Locate every blood parasite and identify its species.
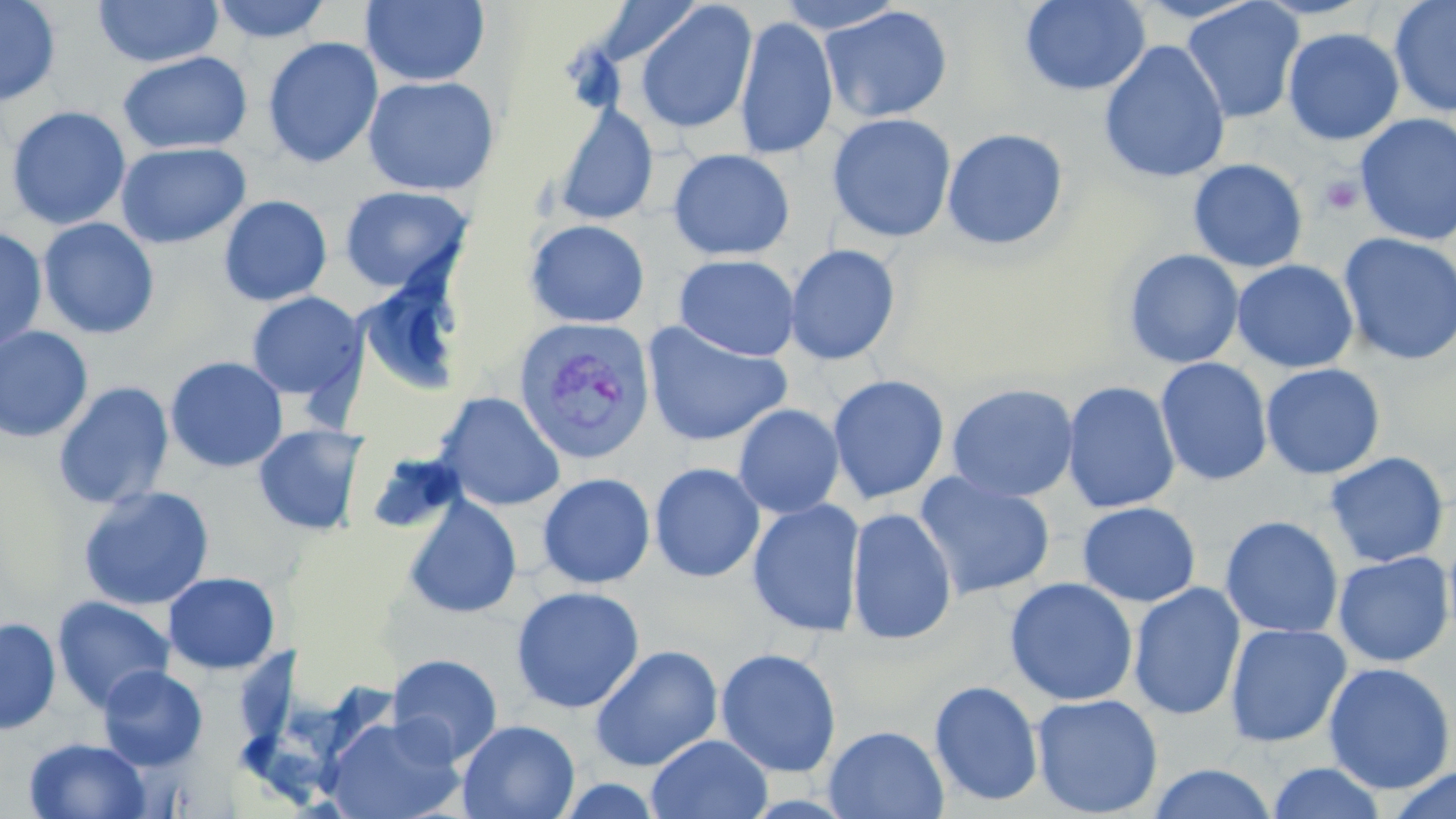

Approximate bounding boxes as named x1/y1/x2/y2 corners in pixels.
Plasmodium vivax-infected red blood cells: (x1=513, y1=317, x2=655, y2=465).
No Plasmodium falciparum, Plasmodium ovale, Plasmodium malariae, Babesia divergens, or Trypanosoma brucei observed.

slide_level_diagnosis: Plasmodium vivax
uninfected_red_blood_cell_locations: 'approximate bounding boxes as named x1/y1/x2/y2 corners in pixels: (x1=0, y1=0, x2=61, y2=107), (x1=93, y1=0, x2=223, y2=68), (x1=209, y1=0, x2=332, y2=43), (x1=774, y1=0, x2=907, y2=34), (x1=1020, y1=0, x2=1150, y2=96), (x1=1389, y1=0, x2=1456, y2=118), (x1=360, y1=1, x2=490, y2=87), (x1=587, y1=1, x2=708, y2=67), (x1=1181, y1=1, x2=1304, y2=124), (x1=633, y1=2, x2=758, y2=135), (x1=819, y1=5, x2=954, y2=124), (x1=734, y1=15, x2=838, y2=160), (x1=1282, y1=27, x2=1405, y2=146), (x1=262, y1=37, x2=383, y2=169), (x1=1098, y1=40, x2=1231, y2=185), (x1=117, y1=51, x2=253, y2=154), (x1=362, y1=75, x2=500, y2=196), (x1=552, y1=103, x2=659, y2=226), (x1=6, y1=106, x2=132, y2=230), (x1=827, y1=113, x2=957, y2=243), (x1=1355, y1=114, x2=1456, y2=246), (x1=941, y1=127, x2=1069, y2=251), (x1=116, y1=142, x2=251, y2=249), (x1=667, y1=148, x2=794, y2=261), (x1=1188, y1=158, x2=1309, y2=272), (x1=339, y1=185, x2=474, y2=294), (x1=218, y1=195, x2=333, y2=306), (x1=37, y1=217, x2=160, y2=339), (x1=525, y1=219, x2=650, y2=328), (x1=0, y1=227, x2=48, y2=353), (x1=1337, y1=232, x2=1456, y2=366), (x1=785, y1=244, x2=902, y2=366), (x1=1122, y1=248, x2=1244, y2=369), (x1=674, y1=254, x2=800, y2=361), (x1=1232, y1=259, x2=1358, y2=373), (x1=354, y1=273, x2=469, y2=398), (x1=245, y1=292, x2=367, y2=404), (x1=641, y1=320, x2=793, y2=447), (x1=0, y1=325, x2=94, y2=443), (x1=164, y1=356, x2=289, y2=473), (x1=1155, y1=357, x2=1274, y2=487), (x1=1260, y1=363, x2=1386, y2=480), (x1=827, y1=373, x2=950, y2=505), (x1=1062, y1=380, x2=1180, y2=514), (x1=53, y1=381, x2=174, y2=511), (x1=946, y1=382, x2=1080, y2=502), (x1=435, y1=391, x2=566, y2=511), (x1=733, y1=404, x2=845, y2=518), (x1=253, y1=424, x2=369, y2=537), (x1=365, y1=449, x2=466, y2=538), (x1=1324, y1=451, x2=1449, y2=568), (x1=649, y1=462, x2=765, y2=583), (x1=537, y1=472, x2=655, y2=589), (x1=913, y1=472, x2=1055, y2=601), (x1=77, y1=485, x2=215, y2=611), (x1=402, y1=493, x2=522, y2=619), (x1=747, y1=498, x2=866, y2=637), (x1=1077, y1=501, x2=1201, y2=607), (x1=846, y1=507, x2=958, y2=645), (x1=1219, y1=515, x2=1344, y2=639), (x1=1333, y1=551, x2=1455, y2=667), (x1=163, y1=572, x2=281, y2=675), (x1=1004, y1=577, x2=1139, y2=706), (x1=1127, y1=581, x2=1246, y2=722), (x1=511, y1=585, x2=645, y2=714), (x1=52, y1=596, x2=175, y2=713), (x1=0, y1=616, x2=60, y2=734), (x1=1224, y1=622, x2=1351, y2=747), (x1=589, y1=644, x2=723, y2=772), (x1=715, y1=648, x2=841, y2=778), (x1=387, y1=653, x2=504, y2=765), (x1=1322, y1=662, x2=1456, y2=794), (x1=97, y1=665, x2=208, y2=771), (x1=929, y1=679, x2=1044, y2=807), (x1=1031, y1=693, x2=1163, y2=818), (x1=323, y1=714, x2=464, y2=819), (x1=457, y1=719, x2=580, y2=819), (x1=823, y1=725, x2=949, y2=818), (x1=647, y1=733, x2=772, y2=819), (x1=23, y1=737, x2=153, y2=819), (x1=1265, y1=762, x2=1388, y2=819), (x1=1145, y1=763, x2=1279, y2=819), (x1=1385, y1=766, x2=1456, y2=818)'
preparation: thin blood smear
magnification: 1000x
modality: light microscopy
image_size: 1456×819 pixels
stain: May-Grünwald-Giemsa
field_of_view: single
platelet_locations: 'approximate bounding boxes as named x1/y1/x2/y2 corners in pixels: (x1=1318, y1=175, x2=1364, y2=216)'